Report the malaria status of this cell.
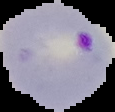

Parasitized.

The area outside the segmented cell region is set to black. Image is 115×112 pixels. From a thin blood film.